Comment on the morphology of the red blood cells.
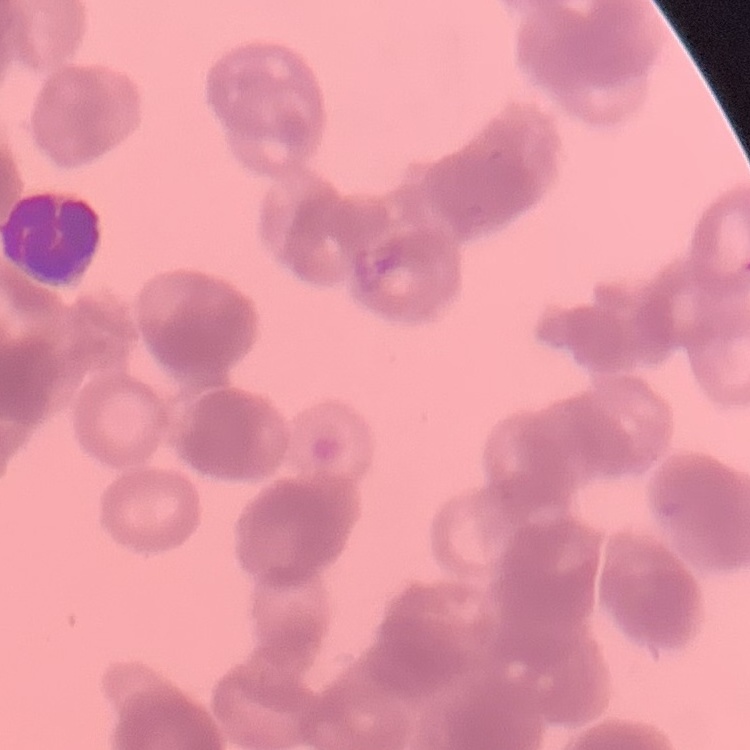
Rouleaux formation.

Thin blood film. Square crop of a larger photomicrograph. Field's or Giemsa stain.